Outline each uninfected red blood cell.
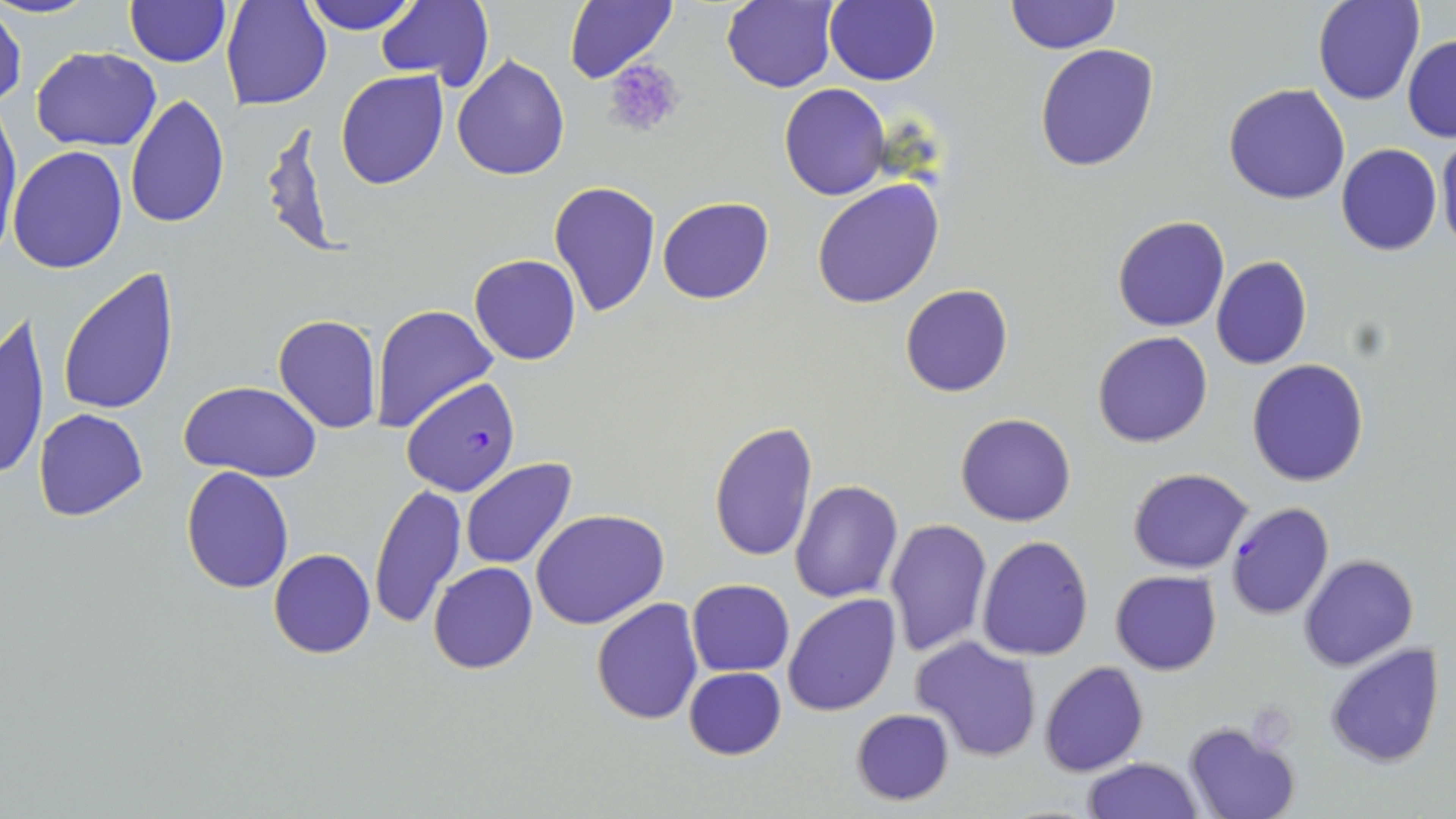

Approximate bounding boxes as (x1, y1, x2, y2) in pixels.
Uninfected red blood cells: (0, 0, 100, 19), (221, 0, 332, 111), (302, 0, 418, 33), (375, 0, 492, 85), (564, 0, 679, 85), (721, 0, 839, 91), (826, 0, 939, 85), (1005, 0, 1119, 54), (1313, 0, 1424, 105), (125, 1, 229, 67), (1, 5, 26, 111), (1403, 35, 1456, 143), (1035, 43, 1160, 173), (31, 47, 162, 151), (452, 55, 570, 180), (336, 70, 448, 189), (778, 83, 889, 200), (1224, 83, 1349, 205), (124, 93, 229, 230), (0, 102, 22, 257), (262, 116, 344, 261), (1437, 129, 1456, 255), (1336, 143, 1442, 255), (8, 145, 128, 273), (811, 178, 944, 309), (548, 181, 661, 319), (658, 197, 773, 304), (1112, 215, 1230, 331), (468, 254, 581, 365), (1211, 255, 1313, 370), (57, 267, 180, 417), (900, 284, 1013, 398), (371, 303, 498, 435), (0, 311, 50, 485), (272, 313, 383, 436), (1092, 331, 1213, 448), (1246, 358, 1369, 486), (178, 380, 322, 481), (33, 408, 148, 523), (955, 412, 1076, 527), (707, 419, 817, 563), (461, 461, 578, 568), (180, 465, 295, 593), (1127, 468, 1253, 574), (790, 481, 903, 602), (370, 484, 465, 629), (530, 507, 669, 629), (884, 518, 992, 656), (977, 535, 1093, 660), (269, 549, 376, 659), (1298, 554, 1418, 671), (428, 561, 538, 674), (1111, 571, 1220, 675), (687, 580, 794, 675), (783, 593, 900, 716), (591, 597, 704, 724), (909, 635, 1042, 762), (1325, 643, 1444, 768), (1038, 660, 1149, 776), (684, 667, 787, 760), (850, 707, 955, 804), (1183, 722, 1300, 819), (1081, 757, 1204, 819).

slide-level diagnosis = Plasmodium falciparum
image size = 1456×819 pixels
Plasmodium falciparum-infected red blood cell locations = approximate bounding boxes as (x1, y1, x2, y2) in pixels: (404, 378, 522, 497), (1224, 501, 1335, 620)
platelet locations = approximate bounding boxes as (x1, y1, x2, y2) in pixels: (603, 58, 686, 140)
modality = light microscopy
preparation = thin blood film
stain = May-Grünwald-Giemsa
magnification = 1000x
field of view = single